Identify the blood parasite species.
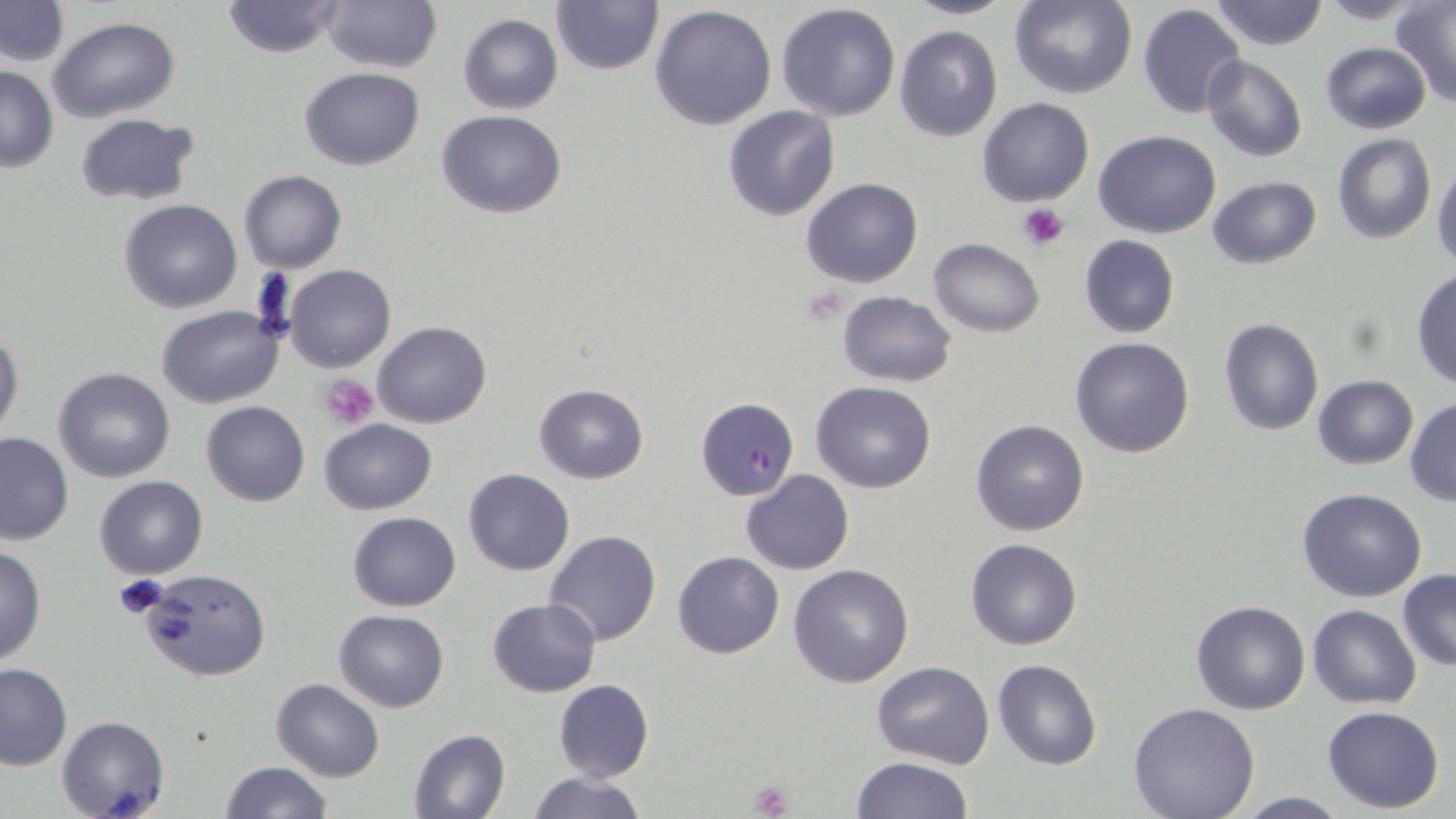
Plasmodium falciparum.

Summary:
  - Coordinate format: approximate bounding boxes as (x1, y1, x2, y2) in pixels
  - Platelet locations: (1018, 203, 1068, 249), (320, 373, 378, 430), (114, 573, 170, 620), (749, 780, 792, 819)
  - Uninfected red blood cell locations: (220, 0, 349, 58), (318, 0, 440, 72), (904, 0, 1016, 20), (1010, 0, 1136, 98), (1210, 0, 1328, 51), (1, 1, 70, 67), (550, 1, 665, 76), (1313, 1, 1428, 24), (777, 2, 901, 121), (1392, 3, 1456, 106), (648, 5, 777, 130), (1138, 5, 1245, 118), (457, 12, 563, 114), (48, 16, 181, 122), (894, 25, 1003, 141), (1319, 41, 1433, 135), (1201, 55, 1307, 162), (0, 65, 57, 171), (299, 66, 424, 169), (977, 98, 1094, 206), (722, 105, 841, 221), (435, 109, 568, 219), (74, 111, 202, 207), (1093, 129, 1222, 238), (1332, 133, 1436, 243), (1431, 164, 1456, 267), (239, 171, 347, 273), (1206, 176, 1320, 270), (800, 177, 923, 288), (117, 200, 243, 314), (1079, 234, 1180, 339), (929, 237, 1044, 337), (282, 263, 396, 372), (1412, 268, 1456, 389), (835, 291, 955, 387), (156, 305, 283, 408), (1218, 317, 1324, 436), (372, 322, 491, 428), (0, 328, 24, 444), (1070, 336, 1196, 458), (54, 367, 175, 481), (1312, 375, 1418, 470), (811, 382, 937, 493), (534, 383, 649, 483), (1405, 398, 1456, 506), (202, 400, 310, 506), (317, 419, 438, 515), (970, 419, 1090, 536), (0, 430, 75, 544), (463, 469, 576, 576), (741, 470, 854, 574), (93, 475, 209, 581), (1297, 489, 1426, 602), (347, 511, 461, 611), (544, 530, 662, 647), (965, 536, 1083, 651), (0, 543, 46, 667), (672, 551, 783, 659), (787, 564, 915, 687), (138, 570, 270, 680), (1398, 570, 1456, 671), (488, 597, 600, 696), (1192, 600, 1309, 715), (1307, 605, 1422, 709), (334, 608, 449, 711), (992, 659, 1103, 771), (871, 660, 994, 768), (0, 663, 73, 770), (271, 678, 384, 782), (553, 679, 654, 783), (1128, 701, 1261, 819), (1322, 706, 1446, 813), (57, 715, 169, 819), (408, 728, 511, 819), (850, 756, 974, 818), (219, 760, 332, 818), (524, 772, 648, 819), (1232, 792, 1354, 818)
  - Plasmodium falciparum-infected red blood cell locations: (695, 396, 799, 501)
  - Preparation: thin blood smear
  - Modality: light microscopy
  - Magnification: 1000x
  - Stain: May-Grünwald-Giemsa
  - Image size: 1456×819 pixels
  - Field of view: one of a larger specimen